Give the extent of all Plasmodium falciparum-infected red blood cells.
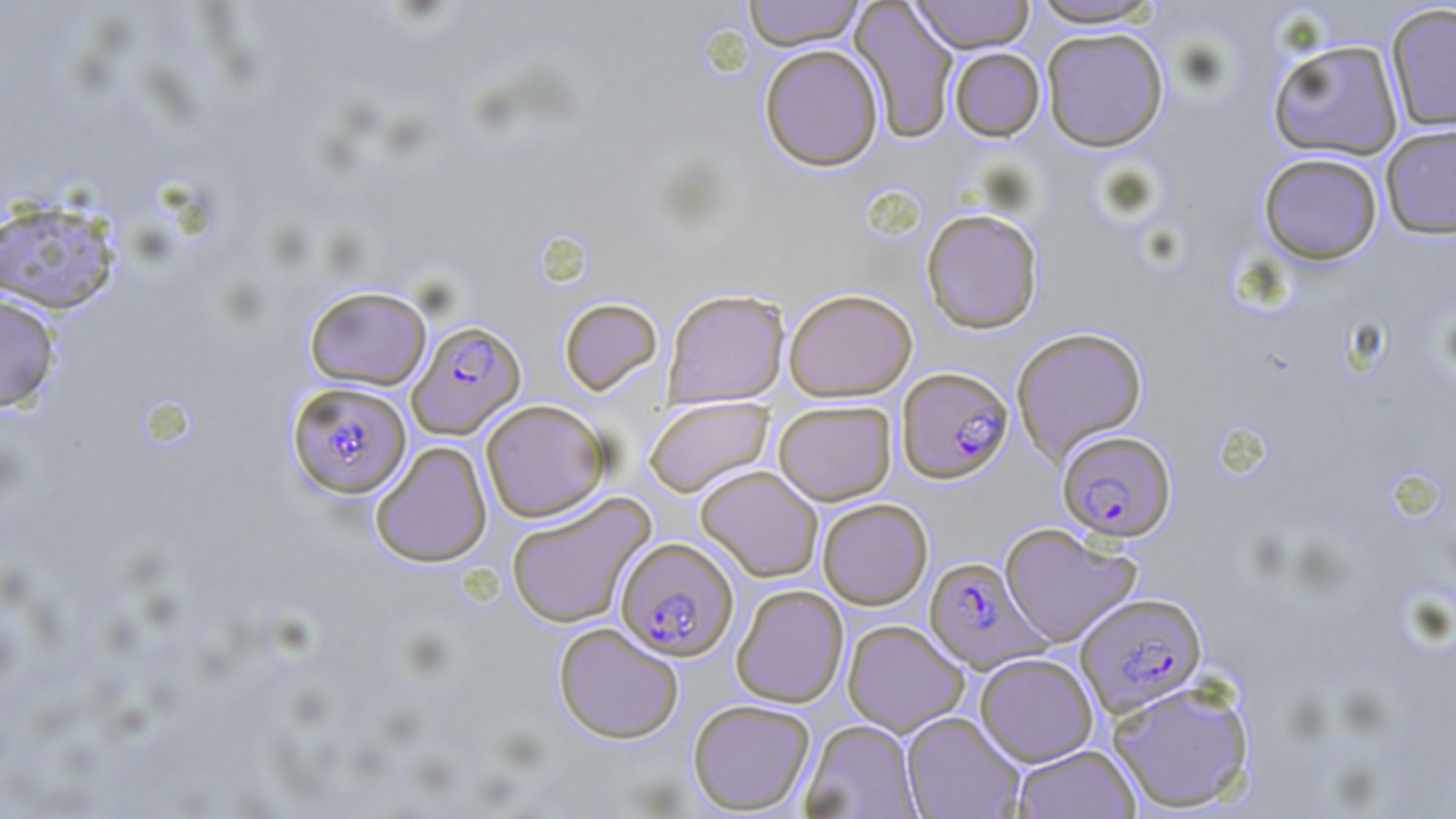

Approximate bounding boxes as (x1,y1)-(x2,y2) corner pairs in pixels.
Plasmodium falciparum-infected red blood cells: (407,319)-(526,438), (898,366)-(1013,484), (287,381)-(412,498), (1056,429)-(1176,542), (616,537)-(739,660), (923,556)-(1048,674), (1075,592)-(1208,716).

Uninfected red blood cell locations: (742,0)-(866,50), (908,0)-(1036,54), (1026,0)-(1166,28), (850,1)-(960,143), (1385,3)-(1456,133), (1041,27)-(1169,151), (1267,38)-(1404,160), (759,44)-(884,171), (949,47)-(1045,141), (1380,123)-(1456,239), (1258,152)-(1383,264), (0,197)-(121,314), (921,207)-(1044,334), (304,285)-(432,390), (663,288)-(790,407), (784,288)-(918,401), (0,292)-(61,413), (559,298)-(662,395), (1011,326)-(1148,464), (644,396)-(773,497), (480,399)-(610,522), (773,400)-(896,506), (370,441)-(492,567), (695,465)-(824,582), (506,492)-(656,628), (817,498)-(933,610), (999,522)-(1142,647), (731,584)-(849,708), (842,619)-(969,736), (553,622)-(683,743), (975,652)-(1098,766), (1106,678)-(1255,813), (688,698)-(816,815), (901,711)-(1025,819), (802,719)-(921,818), (1013,744)-(1140,819). Slide-level diagnosis: Plasmodium falciparum. Thin blood smear. Image is 1456×819 pixels. Captured at 1000x magnification. May-Grünwald-Giemsa stain. Single field of view. Optical microscopy.